Assess the morphology of the red blood cells.
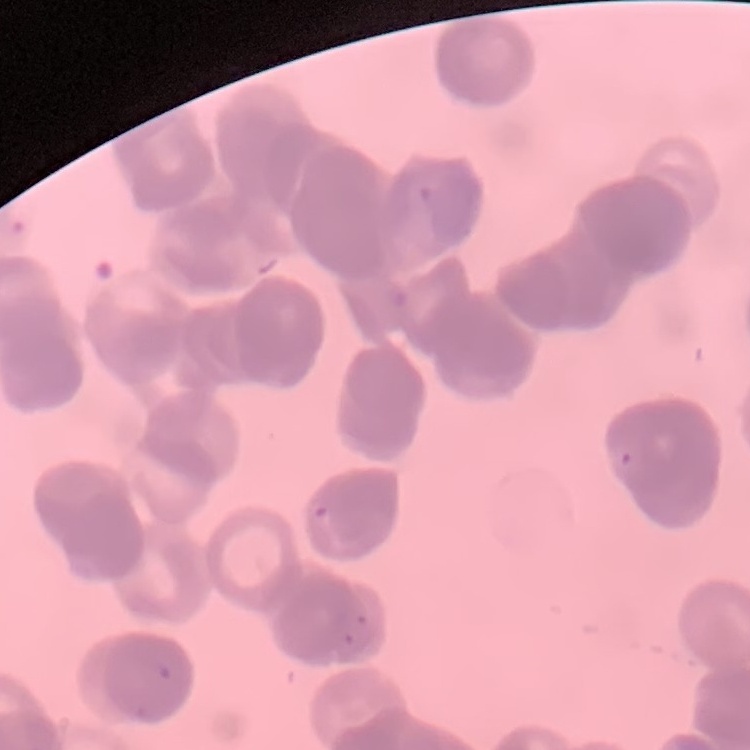

Rouleaux formation.

Summary:
  - Stain: Field's or Giemsa
  - Image type: square crop of a larger photomicrograph
  - Preparation: thin blood film